State the blood parasite species.
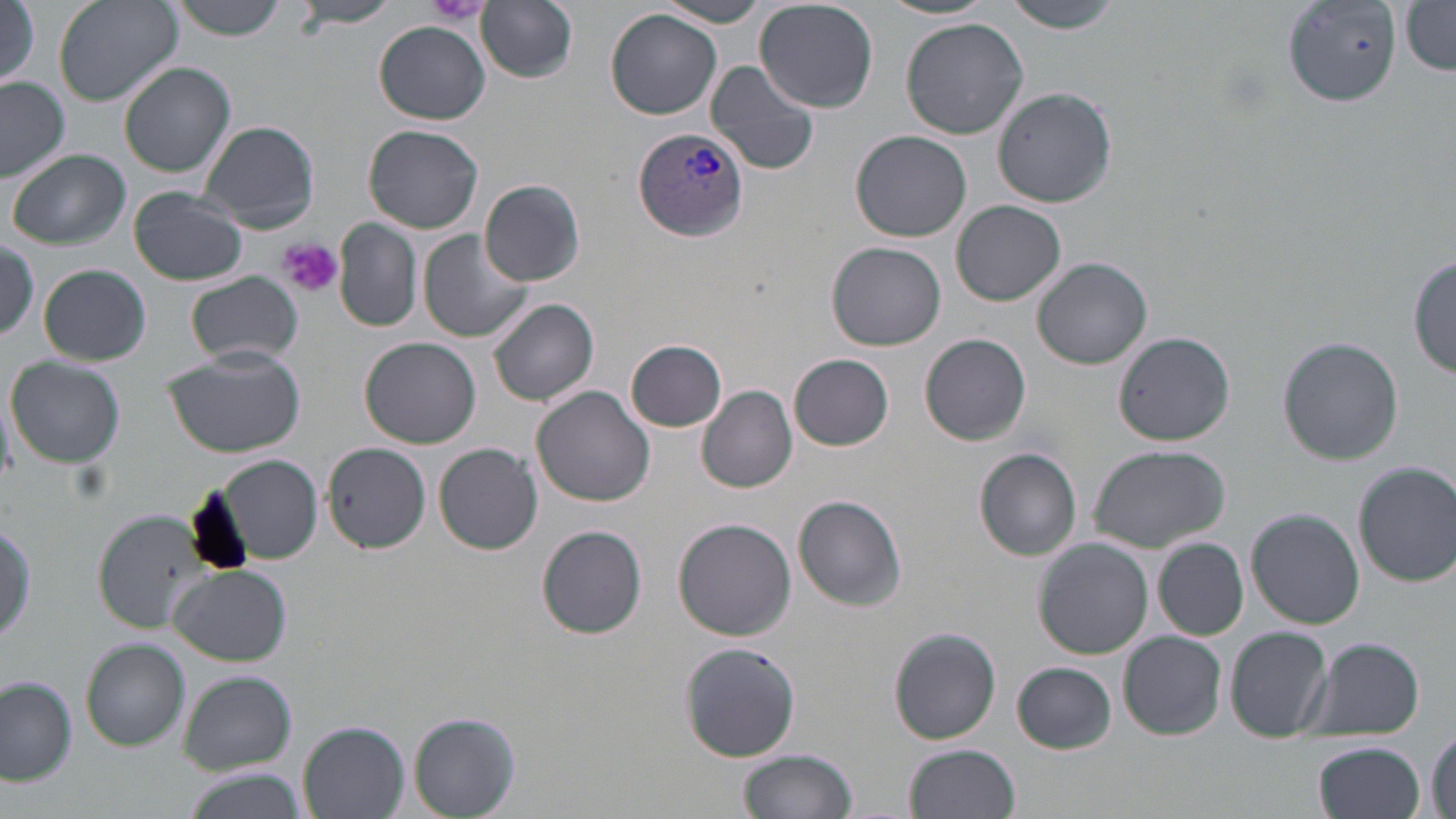
Plasmodium vivax.

{
  "stain": "May-Grünwald-Giemsa",
  "magnification": "1000x",
  "preparation": "thin blood film",
  "field_of_view": "one of a larger specimen",
  "uninfected_red_blood_cell_locations": "approximate bounding boxes as (x1, y1, x2, y2) in pixels: (53, 0, 180, 105), (167, 0, 291, 40), (1005, 0, 1126, 32), (477, 1, 578, 84), (753, 1, 879, 112), (880, 1, 994, 22), (1, 2, 39, 91), (293, 2, 403, 28), (653, 2, 771, 27), (1284, 2, 1399, 105), (1400, 3, 1456, 74), (605, 9, 724, 120), (900, 18, 1028, 138), (375, 21, 489, 124), (703, 59, 822, 176), (118, 61, 236, 177), (0, 78, 69, 182), (991, 88, 1116, 208), (198, 119, 320, 232), (364, 124, 484, 234), (850, 131, 972, 243), (8, 149, 130, 251), (480, 180, 585, 287), (127, 188, 248, 287), (952, 200, 1066, 305), (335, 218, 421, 333), (418, 231, 532, 343), (1, 239, 39, 342), (826, 242, 946, 350), (1410, 255, 1456, 378), (1032, 258, 1153, 369), (40, 264, 149, 365), (186, 272, 304, 365), (488, 295, 600, 406), (1115, 330, 1236, 445), (920, 333, 1032, 444), (1278, 336, 1404, 464), (361, 337, 480, 448), (627, 339, 728, 432), (161, 344, 305, 456), (789, 353, 894, 451), (7, 358, 126, 468), (700, 385, 798, 493), (531, 387, 656, 508), (322, 441, 431, 554), (434, 442, 543, 555), (1088, 444, 1228, 552), (974, 448, 1082, 561), (220, 455, 323, 563), (1354, 461, 1456, 586), (791, 496, 907, 611), (1246, 508, 1364, 627), (90, 515, 221, 642), (673, 518, 796, 641), (537, 525, 647, 639), (1154, 538, 1250, 639), (1033, 539, 1154, 659), (170, 565, 291, 665), (1226, 626, 1332, 739), (890, 627, 1002, 744), (1118, 631, 1227, 739), (1300, 635, 1425, 742), (80, 637, 190, 751), (680, 643, 801, 763), (1013, 662, 1118, 753), (179, 671, 295, 772), (0, 678, 78, 786), (409, 711, 521, 817), (299, 722, 410, 819), (1428, 727, 1455, 819), (1313, 741, 1428, 819), (904, 744, 1020, 819), (738, 749, 859, 819), (179, 767, 303, 819)",
  "image_size": "1456×819 pixels",
  "platelet_locations": "approximate bounding boxes as (x1, y1, x2, y2) in pixels: (423, 0, 491, 27), (278, 238, 343, 298)",
  "modality": "optical microscopy",
  "plasmodium_vivax_infected_red_blood_cell_locations": "approximate bounding boxes as (x1, y1, x2, y2) in pixels: (632, 128, 750, 242)"
}